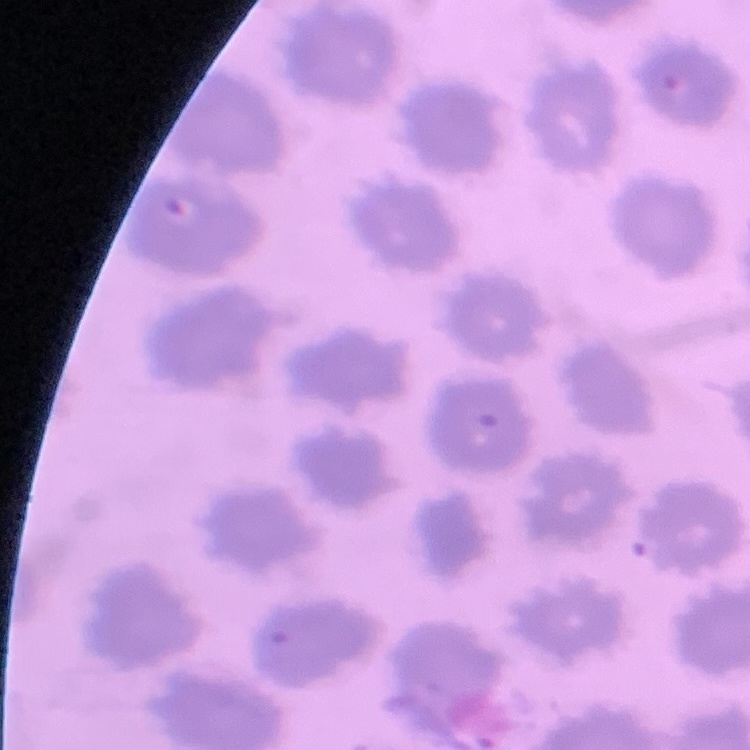
Summary:
  - Erythrocyte morphology: no rouleaux formation
  - Preparation: thin blood smear
  - Image type: square crop of a larger photomicrograph
  - Stain: Field's or Giemsa